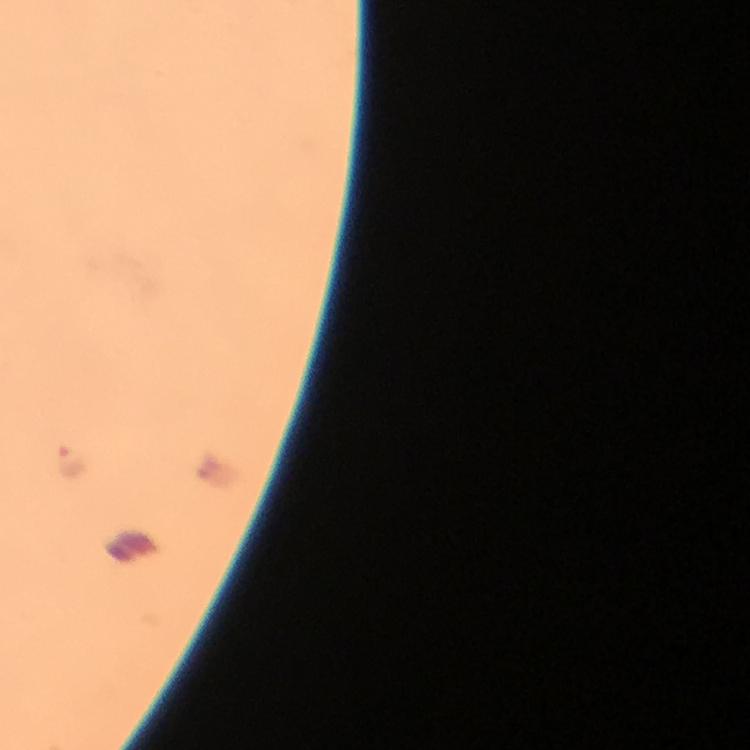

Approximate centers as {x, y} in pixels. Malaria parasite locations: {70, 463}. From a malaria diagnostic workup. 100x magnification. Cropped region of a single field of view. Smartphone photograph taken through a microscope. Immersion oil applied. Giemsa stain. Image is 750×750 pixels. Thick blood smear.